Look for Plasmodium parasites.
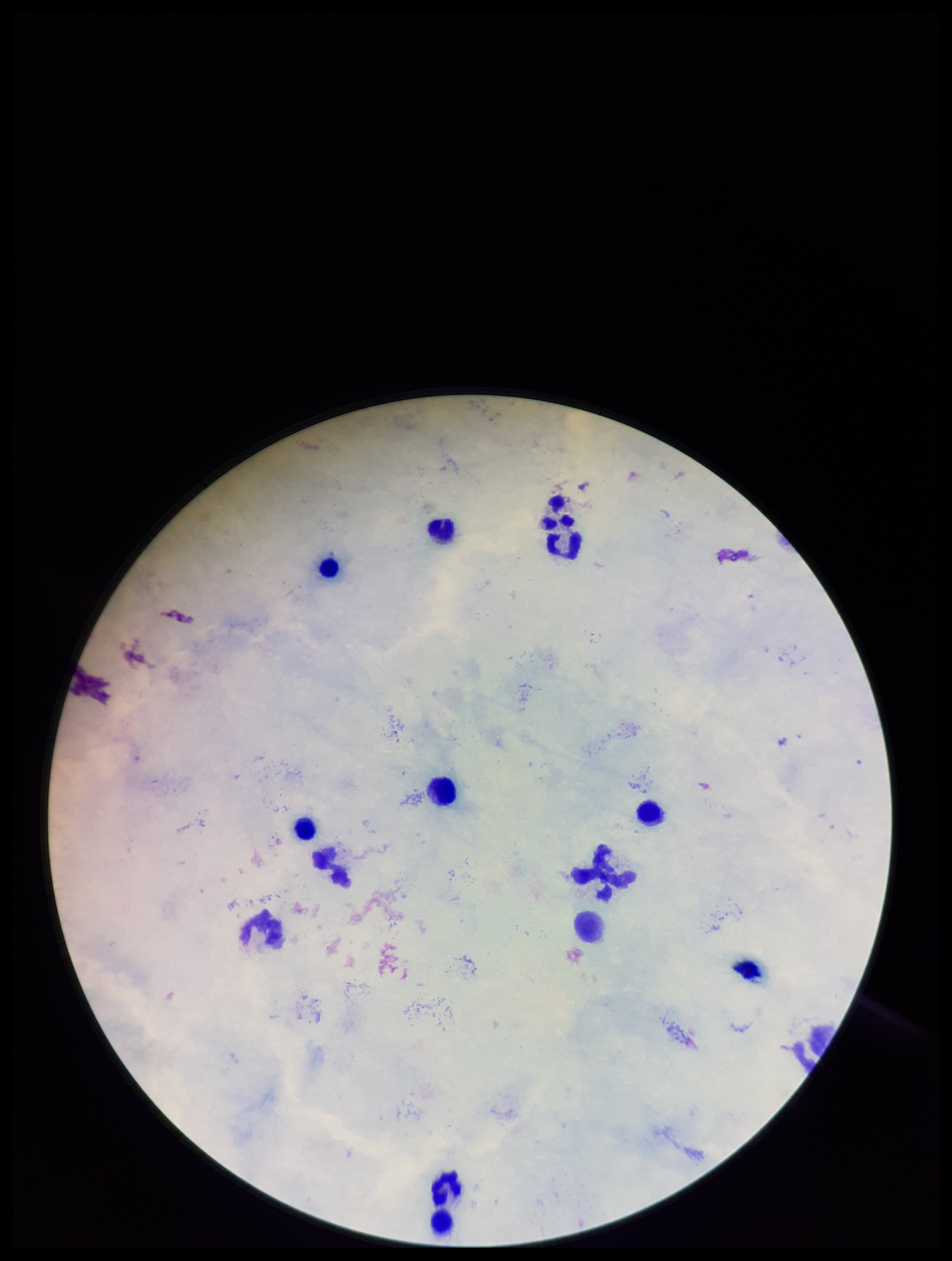
None identified.

Summary:
  - Preparation: thick
  - Image size: 952×1261 pixels
  - Capture: smartphone photograph through the microscope eyepiece
  - Patient malaria status: negative
  - Stain: Giemsa
  - Field of view: one from this slide
  - Leukocyte count: 13
  - Parasite count: 0